Identify the cell.
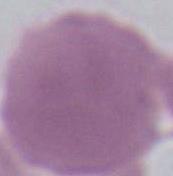
An erythrocyte.

Summary:
  - Modality: micrograph
  - Magnification: 1000x